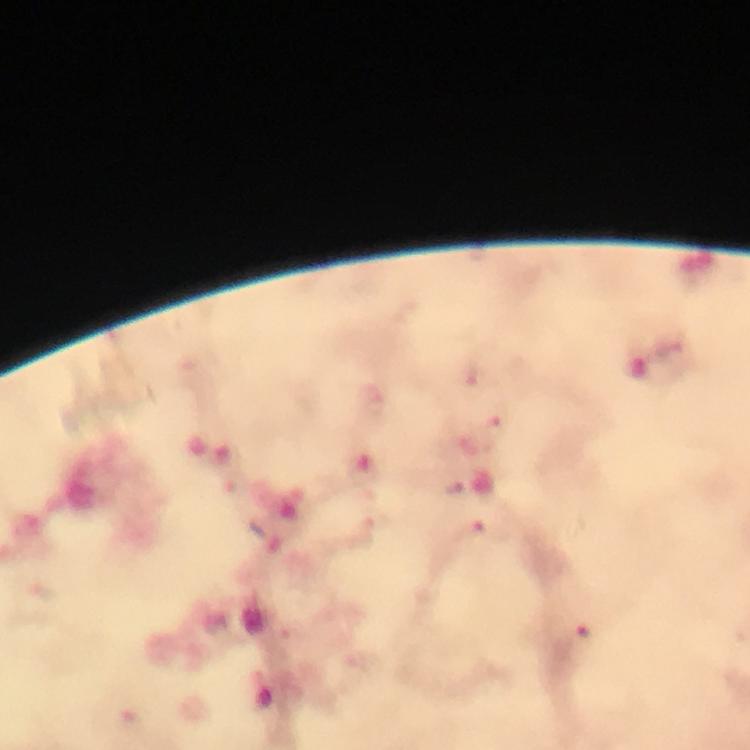
Approximate object centers, in pixels from the top-left corner.
Summary:
  - Plasmodium parasite locations: (x=496, y=428), (x=485, y=532), (x=585, y=633), (x=130, y=723)
  - Image size: 750×750 pixels
  - Cropped from: a single field of view
  - Context: from a diagnostic examination for malaria
  - Magnification: 100x
  - Immersion oil: applied
  - Capture: smartphone camera through the microscope
  - Stain: Giemsa
  - Preparation: thick blood smear